Name the blood parasite species.
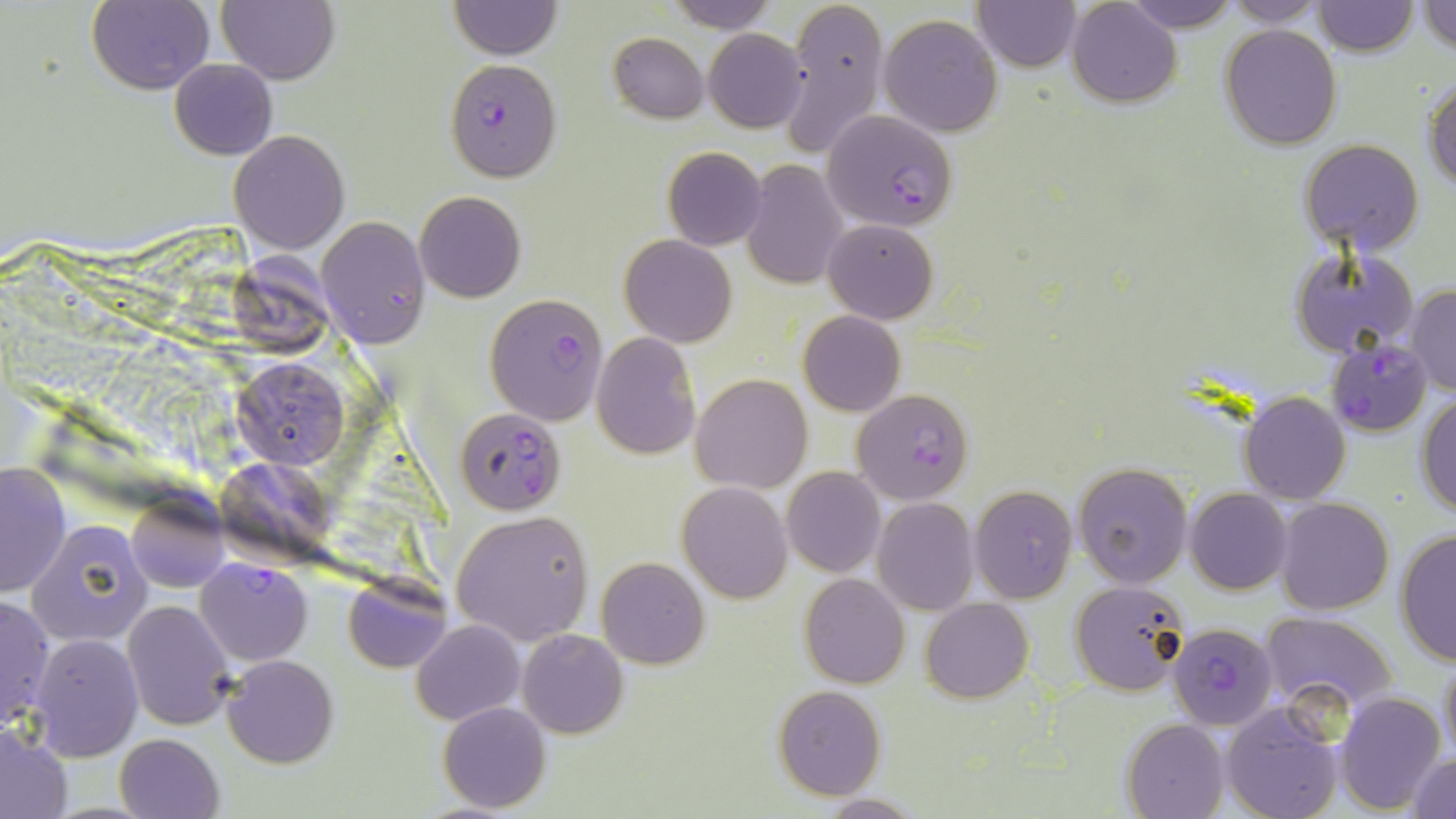

Plasmodium falciparum.

Approximate bounding boxes as (x1, y1, x2, y2) in pixels. Uninfected red blood cell locations: (217, 0, 339, 85), (448, 0, 562, 59), (667, 0, 776, 32), (780, 0, 888, 158), (1067, 0, 1181, 107), (1122, 0, 1241, 33), (1224, 0, 1332, 26), (1310, 0, 1419, 56), (86, 1, 214, 94), (975, 1, 1080, 72), (1418, 1, 1456, 56), (878, 13, 1004, 138), (1220, 25, 1341, 149), (703, 28, 809, 133), (608, 33, 707, 122), (170, 58, 278, 159), (1424, 75, 1456, 195), (229, 130, 348, 254), (1298, 140, 1424, 257), (661, 146, 766, 250), (740, 159, 848, 289), (414, 191, 526, 303), (316, 218, 429, 347), (822, 219, 938, 323), (620, 234, 736, 347), (1288, 246, 1418, 358), (1405, 284, 1456, 397), (798, 311, 905, 416), (591, 333, 701, 460), (233, 358, 348, 469), (691, 374, 811, 493), (1238, 390, 1351, 503), (1417, 393, 1456, 520), (1073, 462, 1193, 589), (1, 463, 72, 596), (221, 467, 336, 561), (781, 467, 885, 578), (677, 482, 791, 602), (970, 485, 1077, 604), (1186, 487, 1292, 594), (125, 496, 228, 594), (872, 497, 978, 614), (1275, 497, 1394, 616), (451, 511, 594, 645), (30, 520, 152, 644), (1395, 529, 1456, 666), (596, 557, 709, 669), (800, 574, 910, 688), (342, 577, 451, 673), (1071, 579, 1190, 698), (0, 593, 55, 731), (922, 598, 1033, 703), (123, 600, 234, 730), (1260, 612, 1397, 716), (412, 620, 524, 724), (518, 629, 628, 739), (25, 633, 143, 760), (1438, 653, 1456, 768), (223, 656, 338, 767), (773, 685, 886, 800), (1335, 692, 1445, 812), (438, 701, 551, 813), (1220, 702, 1344, 819), (1123, 719, 1231, 819), (1, 724, 72, 819), (114, 733, 223, 819), (1404, 754, 1456, 819), (814, 793, 922, 817). Plasmodium falciparum-infected red blood cell locations: (445, 60, 561, 180), (823, 108, 958, 233), (485, 293, 609, 425), (1327, 337, 1431, 437), (852, 388, 975, 504), (460, 415, 562, 514), (195, 558, 312, 666), (1168, 622, 1279, 732). May-Grünwald-Giemsa stain. Image is 1456×819 pixels. Thin blood film. One field of a larger specimen. 1000x magnification. Optical microscopy.